Identify the cell.
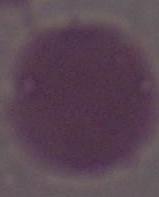

An erythrocyte.

Captured at 1000x magnification. Photomicrograph.